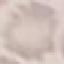
Malaria status: uninfected. Giemsa stain. Thin blood film. Photographed with a smartphone camera at the microscope eyepiece. Cell patch, automatically extracted from a larger field of view and resized to 64 × 64 pixels.